Name the parasite shown.
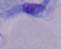

This is a trypanosome.

Photomicrograph. 1000x magnification.